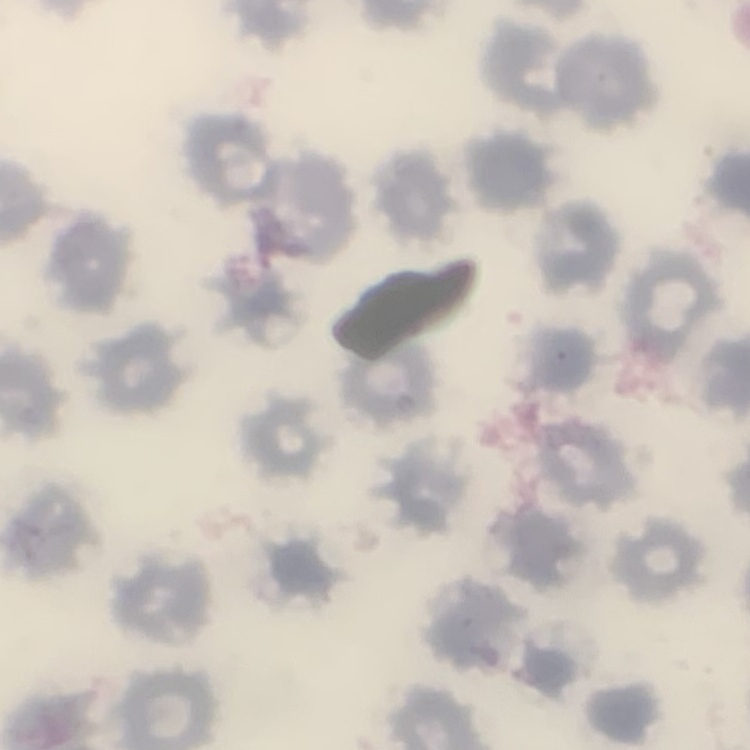

The red blood cells show no rouleaux formation. Square crop of a larger photomicrograph. Thin peripheral smear. Stained with either Field's or Giemsa.